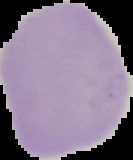
Summary:
  - Malaria status: uninfected
  - Image size: 133×160 pixels
  - Preparation: thin blood film
  - Image type: cell region segmented out of the field of view; surrounding area masked to black